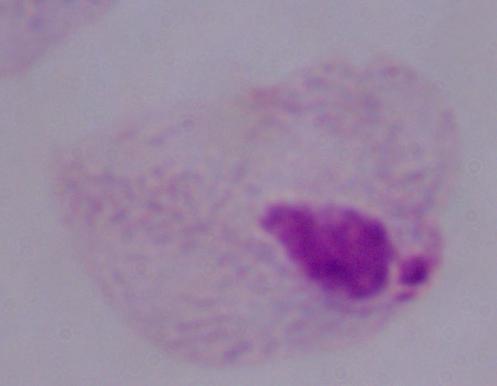

Summary:
  - Modality: micrograph
  - Identification: trichomonad
  - Magnification: 1000x